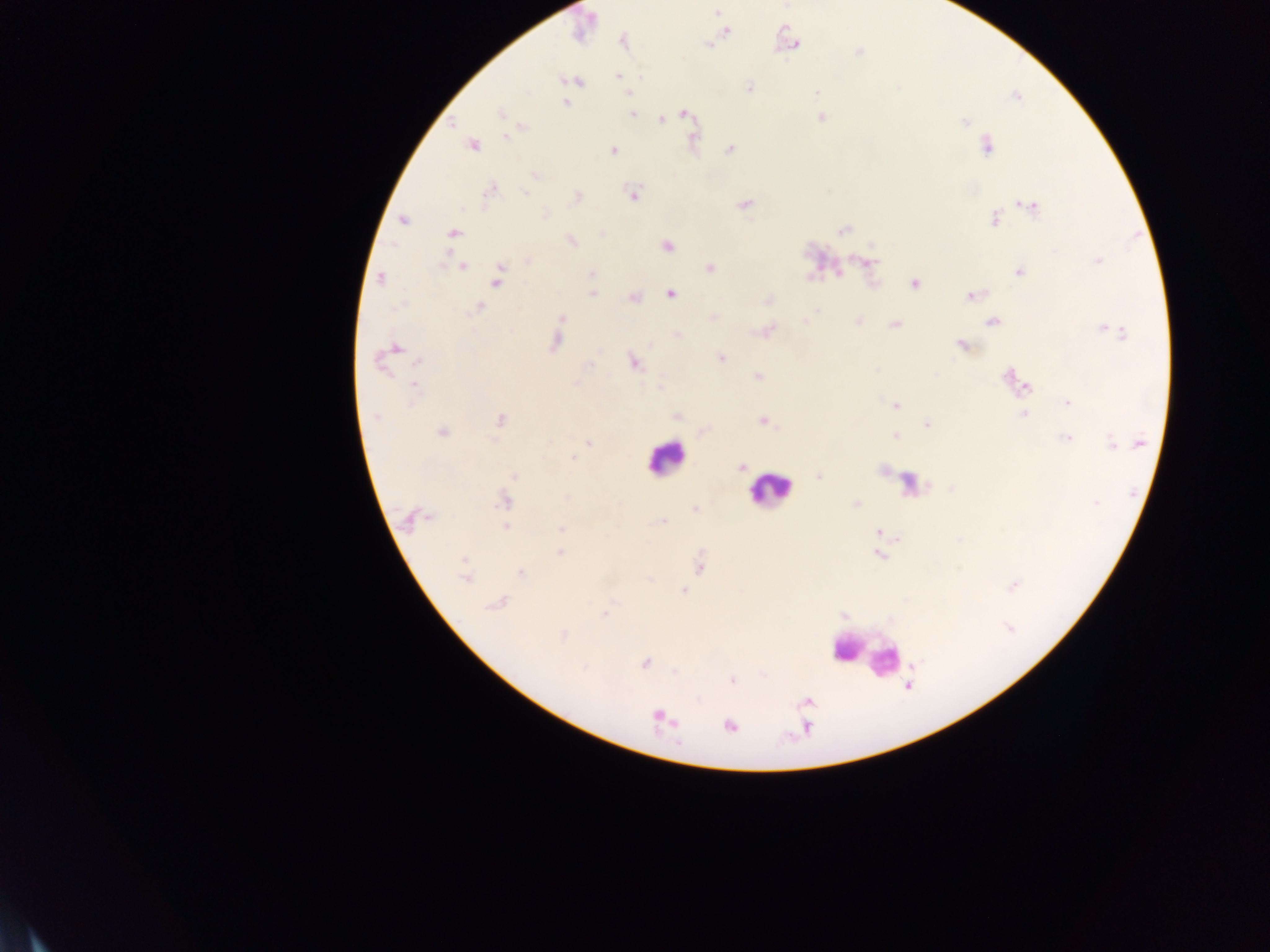
{
  "malaria_parasite_locations": "approximate centers as x y in pixels: 716 12; 727 30; 624 42; 792 43; 709 45; 858 52; 618 76; 574 81; 748 87; 817 93; 1017 97; 565 103; 501 114; 632 114; 686 114; 821 117; 661 120; 964 121; 508 136; 693 137; 473 145; 987 146; 729 150; 613 151; 535 175; 491 192; 526 193; 633 195; 577 197; 744 205; 1030 206; 545 214; 994 219; 402 221; 843 230; 453 232; 571 241; 667 245; 527 261; 1096 261; 869 262; 463 267; 710 268; 839 273; 1019 273; 591 274; 497 277; 380 279; 915 284; 591 294; 670 295; 971 295; 633 297; 767 301; 478 307; 817 310; 562 318; 858 320; 992 322; 894 324; 1110 331; 767 332; 678 335; 555 343; 962 345; 394 348; 721 357; 418 363; 634 363; 591 365; 759 376; 1009 378; 1025 385; 414 386; 660 387; 1068 402; 896 405; 1023 414; 677 416; 377 417; 499 419; 763 421; 926 424; 442 432; 896 436; 1066 438; 588 444; 1112 444; 1139 444; 574 458; 741 468; 514 476; 819 476; 568 497; 504 501; 1096 502; 856 504; 694 509; 427 517; 412 518; 663 521; 505 526; 561 528; 878 532; 559 553; 878 555; 463 561; 700 568; 521 573; 464 577; 1013 586; 684 590; 497 603; 605 614; 1009 627; 563 635; 645 663; 583 668; 732 680; 661 718; 729 726",
  "field_of_view": "single",
  "country": "Ghana",
  "image_size": "1270×952 pixels",
  "capture": "mobile-phone photograph through a microscope",
  "leukocyte_locations": "approximate centers as x y in pixels: 665 458; 768 490; 866 653",
  "preparation": "thick blood smear"
}